Classify this cell by malaria status.
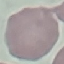

Uninfected.

Automatically extracted cell patch, resized to 64 × 64 pixels. Photographed with a smartphone camera at the microscope eyepiece. Thin blood smear. Giemsa stain.